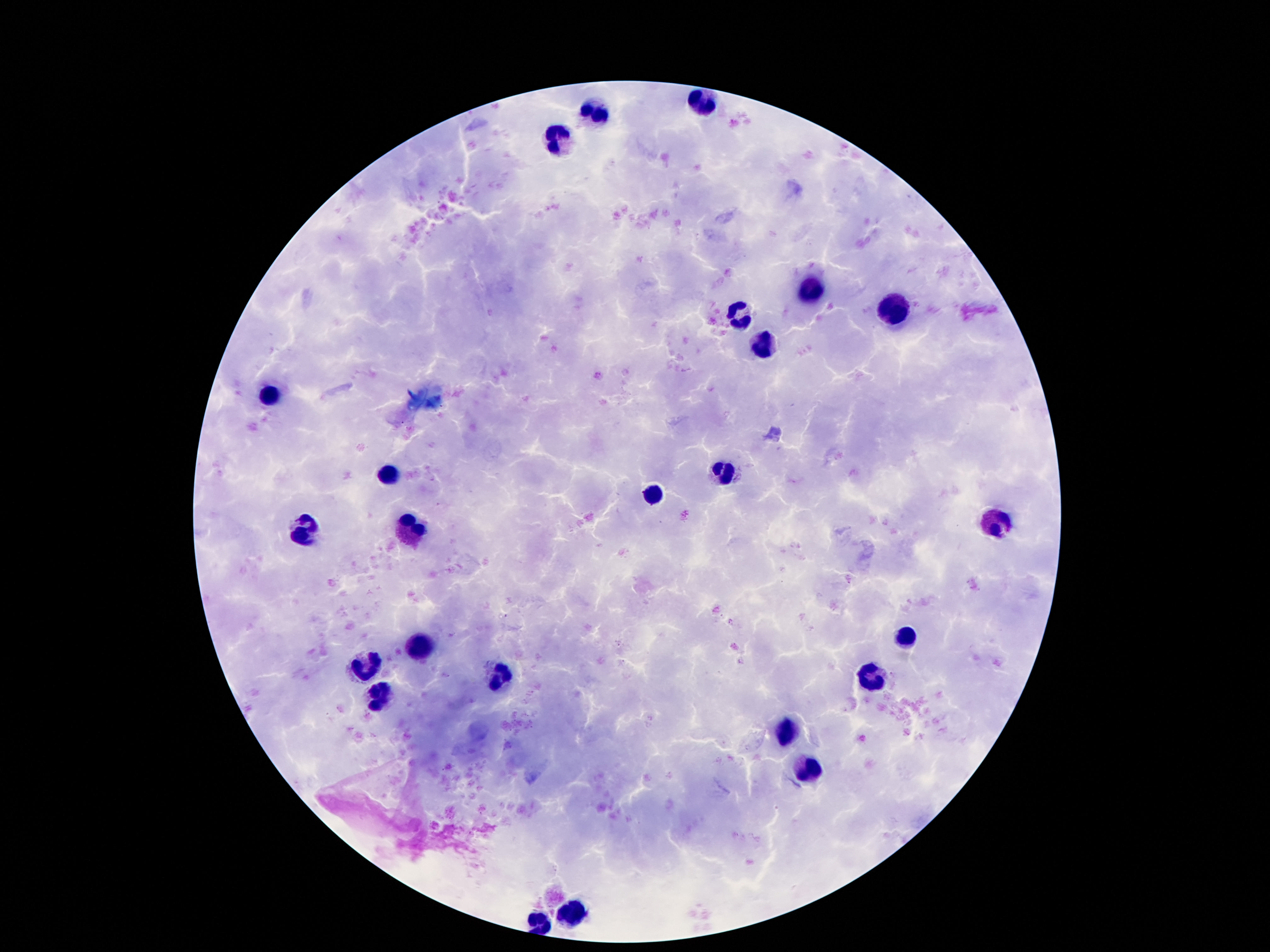

capture: smartphone camera through the microscope eyepiece
image_size: 1270×952 pixels
leukocyte_locations: 'approximate centers as (x, y) in pixels: (706, 104), (601, 111), (557, 139), (813, 289), (897, 312), (742, 318), (765, 348), (269, 396), (723, 472), (387, 474), (656, 495), (996, 524), (412, 527), (305, 533), (906, 637), (419, 648), (364, 666), (872, 675), (498, 677), (377, 695), (786, 730), (809, 772), (572, 908), (540, 922)'
preparation: thick blood smear
magnification: 100x
field_of_view: one from this slide
stain: Giemsa
patient_malaria_status: uninfected